Give the position of every Plasmodium parasite.
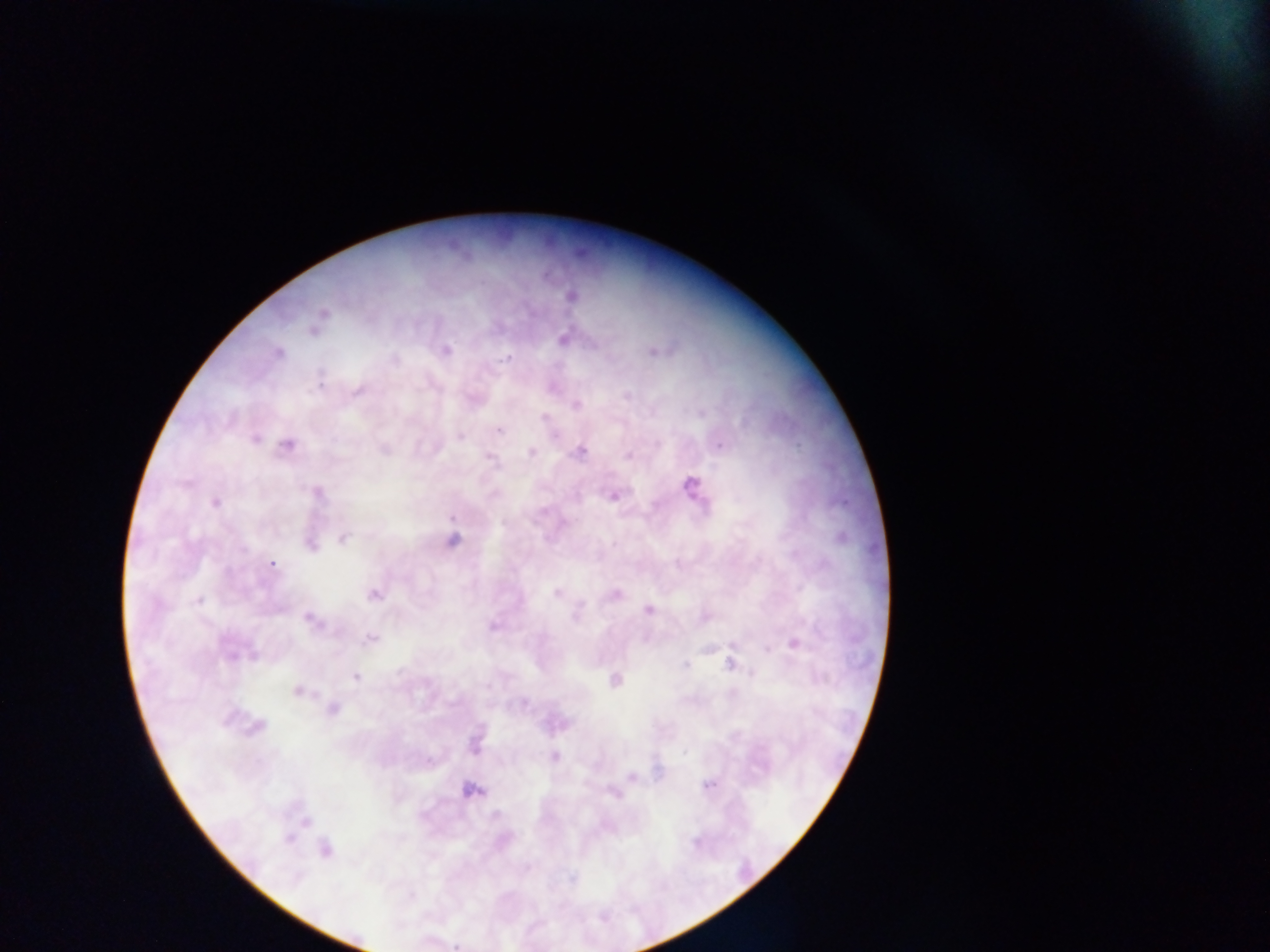

Approximate centers as [x, y] in pixels.
Plasmodium parasites: [571, 296], [323, 313], [313, 331], [564, 339], [446, 351], [653, 352], [279, 353], [507, 357], [395, 360], [320, 381], [357, 391], [627, 396], [576, 404], [543, 417], [499, 429], [459, 437], [255, 439], [287, 445], [720, 446], [384, 450], [580, 451], [531, 452], [628, 456], [491, 458], [185, 484], [691, 485], [317, 494], [614, 496], [215, 502], [451, 517], [342, 539], [452, 541], [310, 544], [272, 564], [557, 593], [616, 594], [373, 595], [198, 601], [581, 606], [648, 610], [310, 620], [493, 627], [370, 639], [795, 644], [232, 655], [730, 664], [686, 665], [355, 676], [615, 680], [297, 691], [523, 702], [333, 709], [257, 727], [684, 753], [554, 756], [631, 776], [708, 785], [472, 789], [615, 794], [495, 815], [288, 839], [696, 842], [325, 849], [572, 878], [457, 947].

image_size: 1270×952 pixels
capture: mobile-phone photograph through a microscope
country: Ghana
preparation: thick blood smear
field_of_view: single